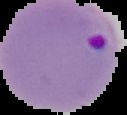

image type = segmented cell region with the area outside set to black
image size = 127×115 pixels
result = Plasmodium parasites identified
preparation = thin blood smear